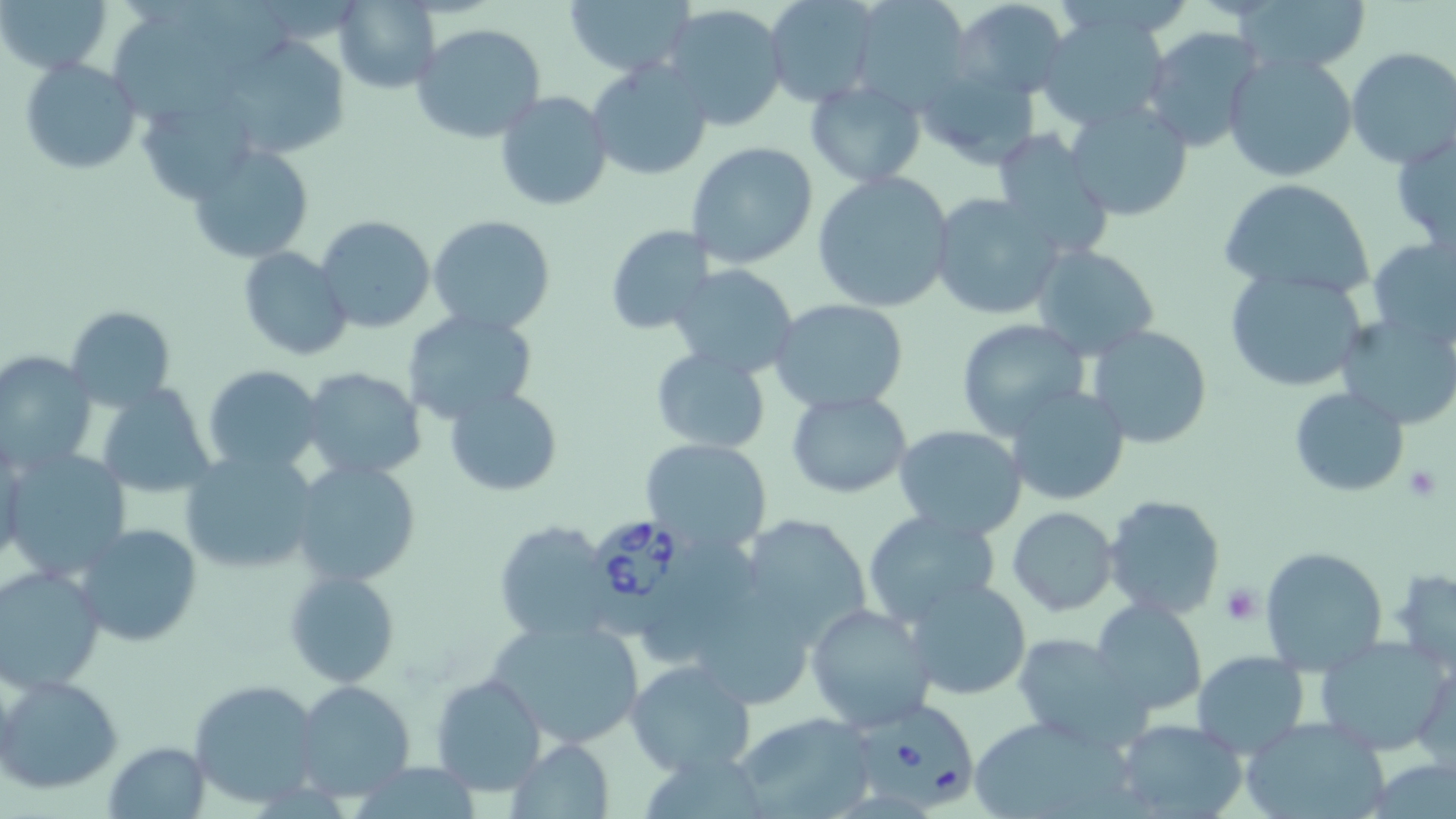

Approximate bounding boxes as (x1,y1)-(x2,y2) corner pairs in pixels. Babesia divergens-infected red blood cell locations: (591,514)-(702,634), (856,696)-(978,811). Uninfected red blood cell locations: (3,0)-(114,75), (333,0)-(441,93), (565,0)-(691,76), (845,0)-(972,109), (951,0)-(1069,99), (1237,0)-(1369,77), (760,1)-(880,107), (658,3)-(790,133), (1033,9)-(1174,132), (117,11)-(245,122), (412,22)-(546,143), (1141,28)-(1264,155), (215,35)-(350,160), (1345,47)-(1456,170), (1223,50)-(1357,184), (18,56)-(142,175), (586,58)-(714,183), (913,64)-(1040,168), (804,79)-(926,186), (495,90)-(614,211), (142,100)-(258,201), (1064,101)-(1193,222), (1390,126)-(1456,252), (989,132)-(1116,261), (686,141)-(817,268), (187,143)-(314,264), (811,170)-(957,312), (1217,178)-(1376,301), (930,191)-(1068,321), (428,214)-(558,337), (317,215)-(435,333), (604,224)-(715,336), (1368,234)-(1456,347), (1031,244)-(1160,359), (240,248)-(352,362), (667,263)-(801,380), (1224,267)-(1370,394), (767,297)-(910,415), (66,304)-(178,411), (401,309)-(538,425), (1336,313)-(1456,429), (954,320)-(1094,440), (1085,325)-(1212,450), (650,347)-(772,454), (0,349)-(99,475), (202,363)-(326,476), (299,367)-(427,482), (97,384)-(217,497), (1005,384)-(1130,506), (1289,386)-(1410,497), (445,387)-(561,496), (786,389)-(914,498), (893,424)-(1027,540), (640,436)-(773,554), (178,448)-(319,576), (5,449)-(133,584), (290,459)-(422,587), (1101,494)-(1226,621), (1008,506)-(1119,616), (863,509)-(1002,626), (737,512)-(874,642), (493,519)-(620,641), (72,523)-(202,647), (647,536)-(760,660), (1260,546)-(1388,675), (1,565)-(106,693), (284,567)-(401,687), (1386,567)-(1456,674), (905,576)-(1033,702), (1091,600)-(1210,718), (705,601)-(808,701), (805,603)-(935,734), (486,614)-(644,752), (1010,631)-(1146,748), (1314,636)-(1454,755), (1191,649)-(1309,757), (1412,655)-(1454,768), (624,658)-(756,779), (430,670)-(548,796), (1,673)-(124,795), (189,680)-(322,807), (294,680)-(415,802), (732,710)-(883,817), (969,714)-(1133,819), (1239,714)-(1393,819), (1114,717)-(1249,818), (506,737)-(614,817), (104,739)-(210,817). Platelet locations: (1403,464)-(1442,501), (1220,584)-(1261,626). Slide-level diagnosis: Babesia divergens. One field of a larger specimen. 1000x magnification. Optical microscopy. May-Grünwald-Giemsa-stained preparation. Thin blood film. Image is 1456×819 pixels.